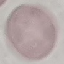

Summary:
  - Result: negative for malaria parasites
  - Stain: Giemsa
  - Capture: smartphone camera at the microscope eyepiece
  - Image type: automatically extracted cell patch, resized to 64 × 64 pixels
  - Preparation: thin blood film